Report the malaria status of this cell.
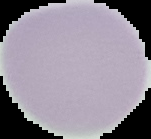

Uninfected.

image_type: segmented cell region on a black background
preparation: thin blood smear
image_size: 151×139 pixels